Name the parasite shown.
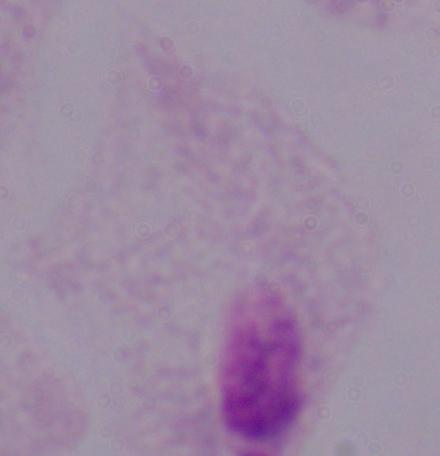

This is a trichomonad.

Summary:
  - Magnification: 1000x
  - Modality: micrograph